Outline every Plasmodium parasite.
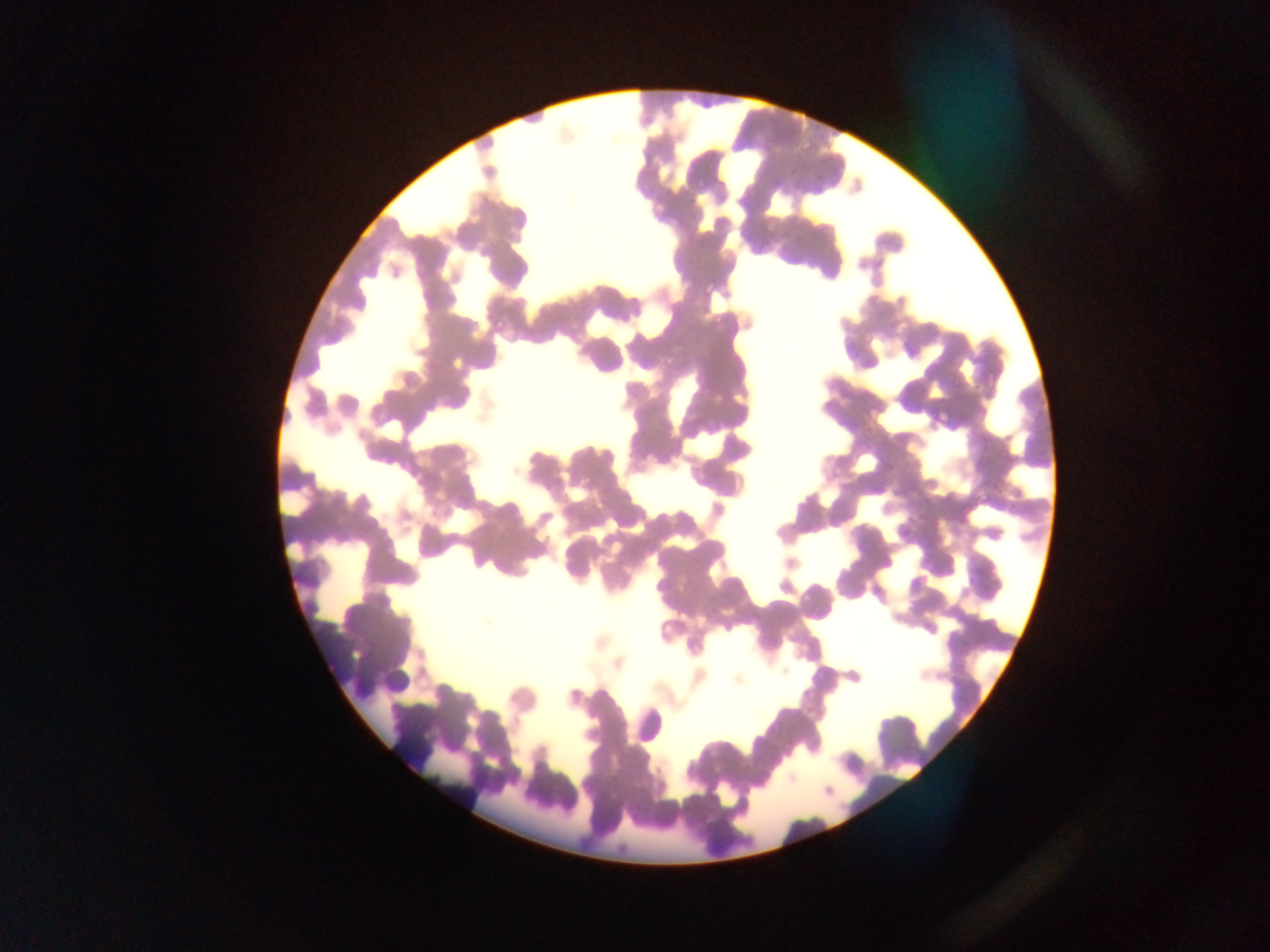

Approximate bounding boxes as left top right bottom in pixels.
Plasmodium parasites: 800 140 815 156; 771 174 786 190; 693 177 709 193; 634 179 649 195; 810 185 826 201; 488 310 507 333; 709 314 728 334; 931 409 951 429; 499 526 513 542.

{
  "capture": "mobile-phone photograph through a microscope",
  "preparation": "thin blood film",
  "image_size": "1270×952 pixels",
  "leukocyte_locations": "approximate bounding boxes as left top right bottom in pixels: 383 663 411 693; 631 706 664 749",
  "field_of_view": "single",
  "country": "Ghana"
}